Describe the morphology of the red blood cells.
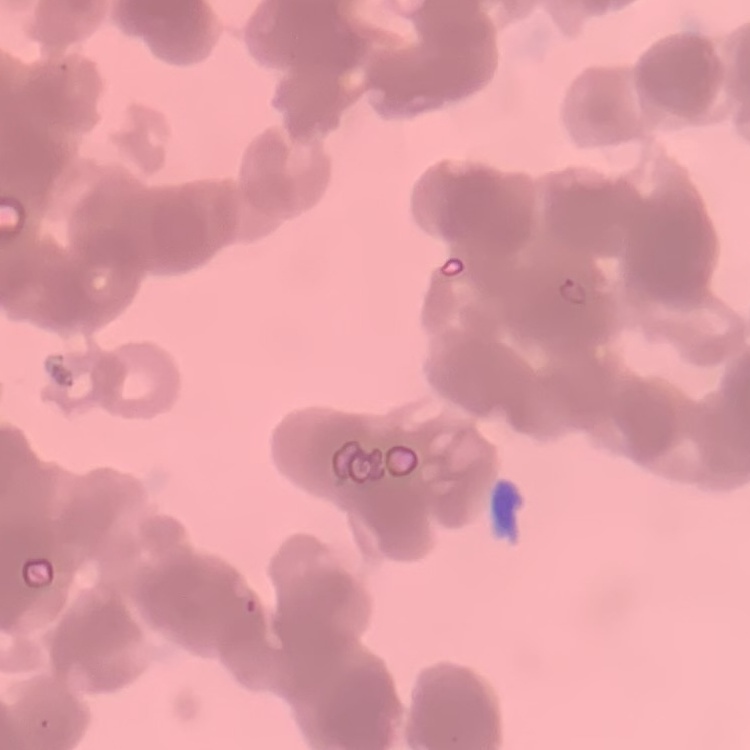

Rouleaux formation.

Square crop of a larger photomicrograph. Stained with either Field's or Giemsa. Thin peripheral smear.